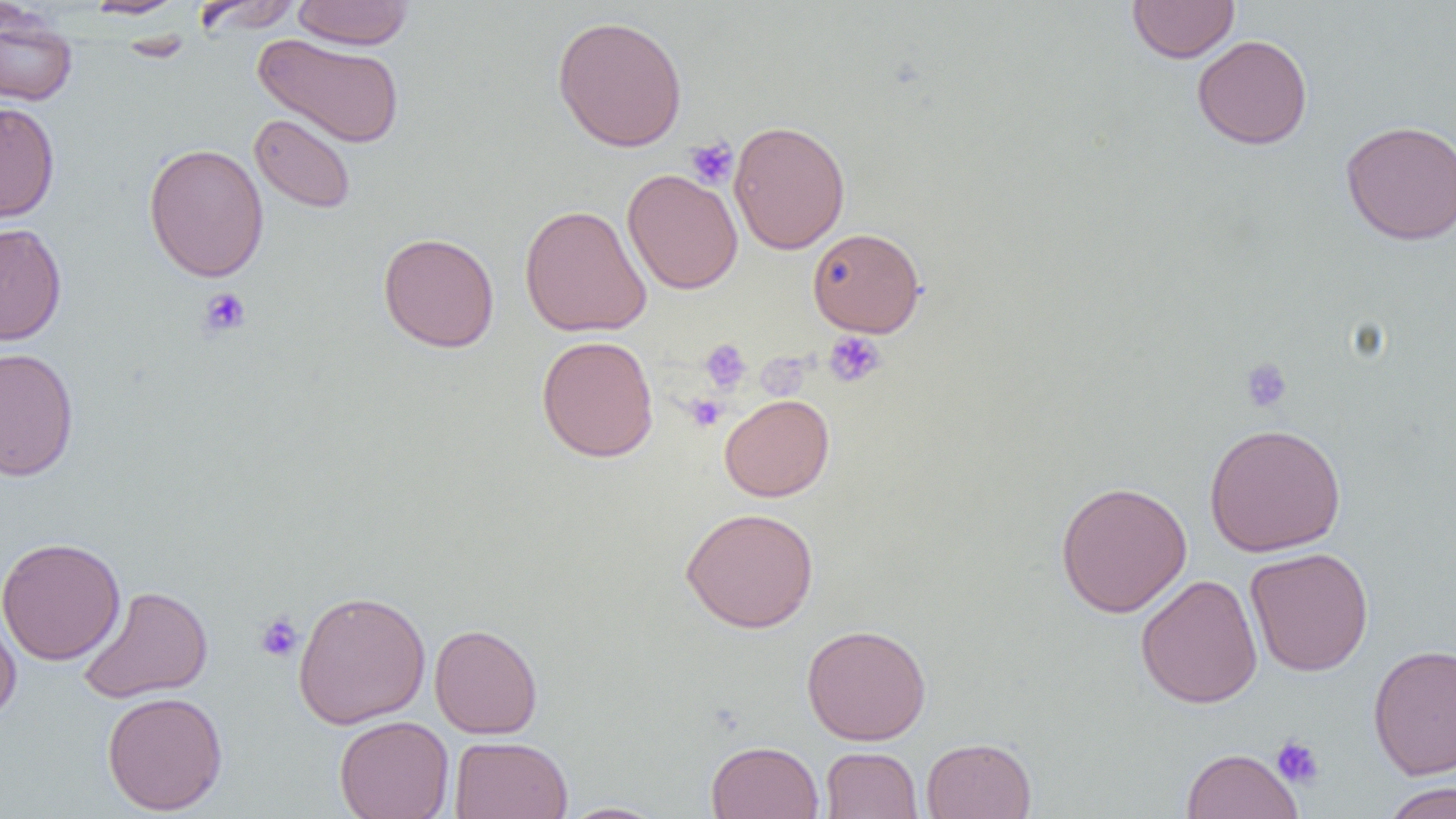

Summary:
  - Coordinate format: approximate bounding boxes as (x1, y1, x2, y2) in pixels
  - Platelet locations: (685, 137, 738, 189), (198, 287, 252, 338), (823, 330, 887, 388), (699, 338, 752, 393), (761, 345, 816, 395), (1239, 357, 1293, 414), (685, 394, 726, 432), (255, 612, 303, 663), (1271, 736, 1325, 789)
  - Uninfected red blood cell locations: (81, 0, 189, 19), (191, 0, 306, 34), (291, 0, 415, 50), (1127, 0, 1239, 63), (0, 6, 78, 108), (552, 15, 688, 152), (252, 34, 405, 148), (1192, 34, 1313, 150), (0, 101, 60, 224), (249, 113, 356, 214), (1340, 119, 1456, 245), (729, 120, 850, 254), (143, 143, 269, 282), (622, 168, 743, 294), (519, 204, 652, 337), (0, 222, 67, 346), (807, 227, 925, 337), (378, 231, 500, 353), (536, 334, 658, 462), (0, 347, 79, 481), (719, 394, 835, 501), (1204, 423, 1346, 556), (1055, 479, 1193, 618), (680, 506, 819, 633), (0, 537, 126, 665), (1245, 547, 1374, 676), (1135, 574, 1263, 709), (76, 586, 213, 703), (292, 588, 431, 729), (0, 603, 22, 725), (801, 623, 931, 745), (429, 624, 543, 738), (1368, 643, 1456, 779), (101, 691, 228, 815), (334, 715, 454, 819), (449, 735, 573, 818), (921, 737, 1036, 819), (706, 740, 824, 819), (820, 747, 923, 818), (1181, 748, 1304, 819), (1381, 782, 1456, 819), (557, 801, 669, 818)
  - Slide-level diagnosis: no evidence of blood parasites
  - Modality: optical microscopy
  - Field of view: single
  - Magnification: 1000x
  - Preparation: thin blood smear
  - Image size: 1456×819 pixels